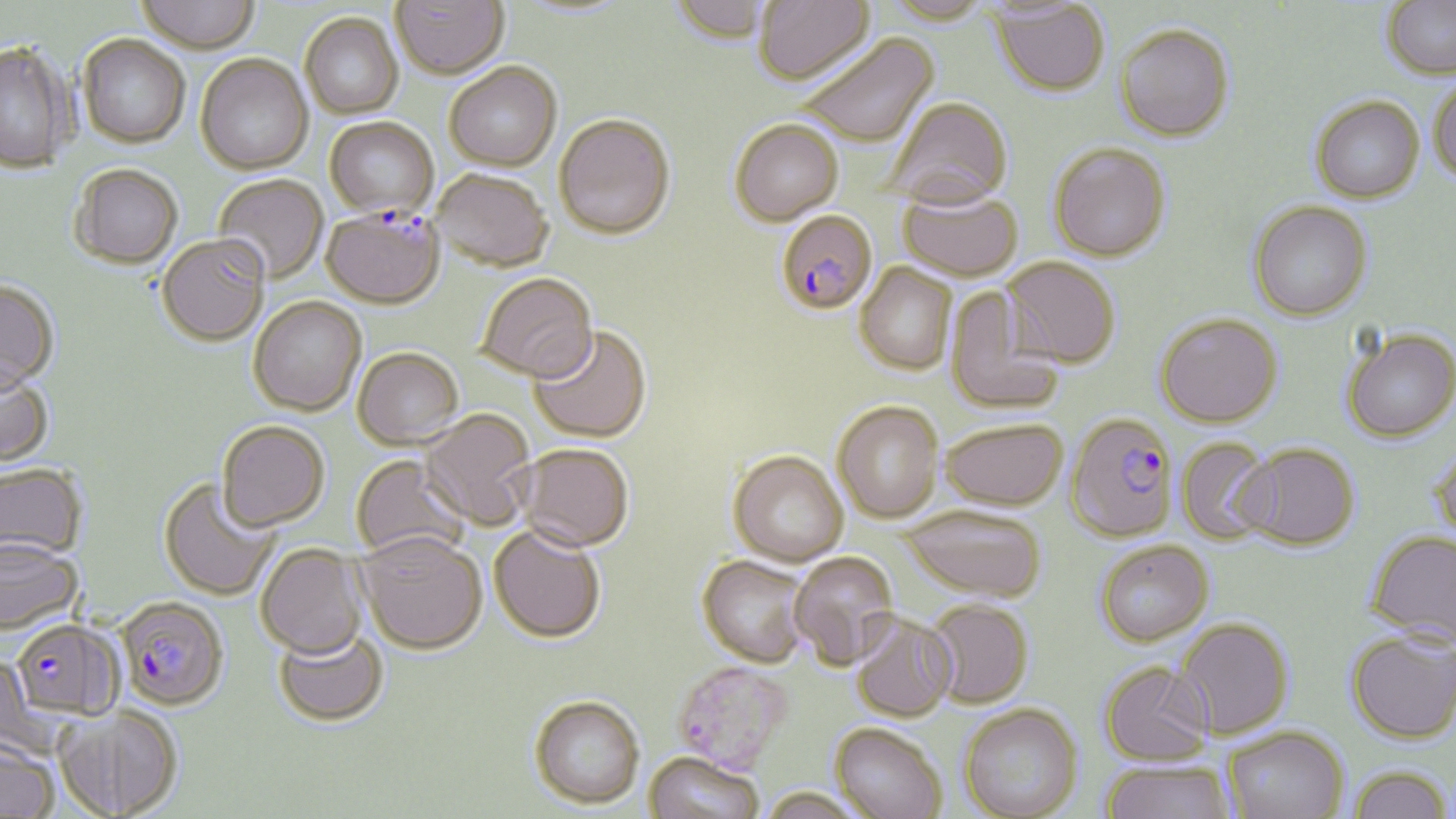
Approximate bounding boxes as named x1/y1/x2/y2 corners in pixels. Platelet locations: (x1=672, y1=660, x2=794, y2=773). Uninfected red blood cell locations: (x1=135, y1=0, x2=260, y2=52), (x1=390, y1=0, x2=509, y2=77), (x1=670, y1=0, x2=773, y2=46), (x1=754, y1=0, x2=875, y2=86), (x1=882, y1=0, x2=994, y2=25), (x1=1381, y1=0, x2=1456, y2=79), (x1=992, y1=2, x2=1110, y2=96), (x1=299, y1=12, x2=404, y2=118), (x1=1115, y1=23, x2=1234, y2=141), (x1=77, y1=33, x2=190, y2=147), (x1=793, y1=33, x2=938, y2=148), (x1=1, y1=40, x2=75, y2=173), (x1=195, y1=53, x2=313, y2=174), (x1=444, y1=62, x2=562, y2=170), (x1=1428, y1=78, x2=1456, y2=186), (x1=1310, y1=95, x2=1425, y2=203), (x1=884, y1=96, x2=1013, y2=208), (x1=553, y1=112, x2=676, y2=238), (x1=324, y1=116, x2=438, y2=217), (x1=730, y1=118, x2=844, y2=224), (x1=1048, y1=142, x2=1171, y2=261), (x1=69, y1=163, x2=183, y2=269), (x1=432, y1=168, x2=554, y2=270), (x1=213, y1=174, x2=329, y2=284), (x1=898, y1=187, x2=1022, y2=280), (x1=1248, y1=200, x2=1373, y2=320), (x1=157, y1=232, x2=270, y2=345), (x1=1003, y1=256, x2=1121, y2=368), (x1=854, y1=262, x2=957, y2=374), (x1=475, y1=272, x2=598, y2=382), (x1=0, y1=278, x2=59, y2=392), (x1=945, y1=287, x2=1063, y2=415), (x1=248, y1=295, x2=367, y2=416), (x1=1156, y1=312, x2=1283, y2=427), (x1=528, y1=324, x2=652, y2=443), (x1=1341, y1=326, x2=1456, y2=442), (x1=353, y1=346, x2=464, y2=449), (x1=0, y1=364, x2=53, y2=466), (x1=832, y1=400, x2=945, y2=523), (x1=419, y1=409, x2=537, y2=531), (x1=940, y1=417, x2=1068, y2=510), (x1=216, y1=419, x2=330, y2=531), (x1=1176, y1=436, x2=1277, y2=544), (x1=514, y1=442, x2=634, y2=550), (x1=1239, y1=443, x2=1359, y2=549), (x1=1428, y1=445, x2=1456, y2=546), (x1=728, y1=450, x2=848, y2=566), (x1=351, y1=454, x2=471, y2=562), (x1=0, y1=463, x2=87, y2=561), (x1=158, y1=477, x2=281, y2=601), (x1=900, y1=504, x2=1047, y2=601), (x1=489, y1=525, x2=607, y2=642), (x1=1365, y1=529, x2=1456, y2=647), (x1=356, y1=530, x2=487, y2=654), (x1=0, y1=538, x2=81, y2=634), (x1=1096, y1=539, x2=1213, y2=646), (x1=256, y1=543, x2=368, y2=659), (x1=789, y1=552, x2=899, y2=670), (x1=697, y1=554, x2=812, y2=667), (x1=925, y1=599, x2=1034, y2=708), (x1=849, y1=612, x2=958, y2=722), (x1=1175, y1=618, x2=1294, y2=739), (x1=273, y1=625, x2=389, y2=726), (x1=1346, y1=629, x2=1456, y2=743), (x1=1100, y1=660, x2=1214, y2=766), (x1=529, y1=694, x2=645, y2=808), (x1=60, y1=703, x2=182, y2=817), (x1=959, y1=703, x2=1083, y2=819), (x1=831, y1=722, x2=948, y2=819), (x1=1223, y1=726, x2=1350, y2=818), (x1=0, y1=739, x2=60, y2=818), (x1=644, y1=750, x2=764, y2=819), (x1=1101, y1=761, x2=1235, y2=819), (x1=1347, y1=765, x2=1453, y2=819), (x1=759, y1=786, x2=867, y2=819). Plasmodium falciparum-infected red blood cell locations: (x1=321, y1=207, x2=445, y2=308), (x1=775, y1=209, x2=878, y2=315), (x1=1070, y1=415, x2=1181, y2=546), (x1=117, y1=595, x2=229, y2=711), (x1=11, y1=618, x2=122, y2=721). Slide-level diagnosis: Plasmodium falciparum. Image is 1456×819 pixels. Thin blood smear. Single field of view. 1000x magnification. May-Grünwald-Giemsa-stained preparation. Optical microscopy.